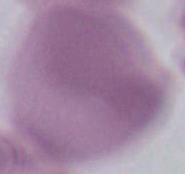
modality = micrograph
identification = erythrocyte
magnification = 1000x